Name the parasite shown.
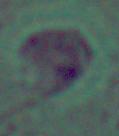

Leishmania.

{
  "magnification": "1000x",
  "modality": "photomicrograph"
}